Locate every blood parasite and identify its species.
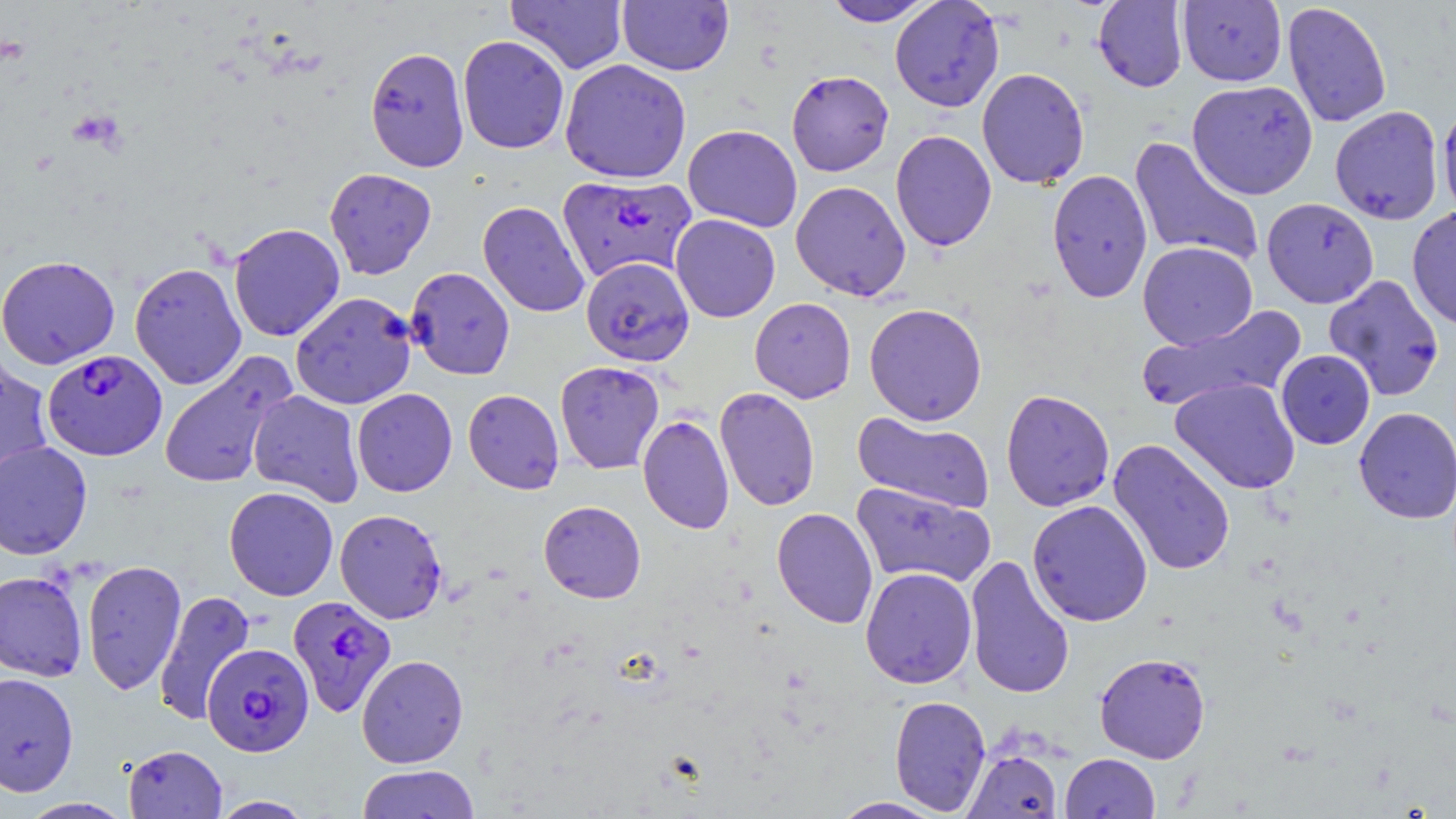
Approximate bounding boxes as (x1,y1)-(x2,y2) corner pairs in pixels.
Plasmodium falciparum-infected red blood cells: (557,174)-(696,283), (42,348)-(167,461), (288,595)-(397,717), (203,644)-(314,756).
No Plasmodium ovale, Plasmodium malariae, Plasmodium vivax, Babesia divergens, or Trypanosoma brucei observed.

Summary:
  - Uninfected red blood cell locations: (822,0)-(936,26), (890,0)-(1005,112), (1093,0)-(1188,92), (1177,0)-(1287,87), (505,1)-(628,74), (617,1)-(734,75), (1282,1)-(1392,128), (457,35)-(570,154), (365,46)-(470,172), (560,58)-(692,183), (976,67)-(1090,189), (786,70)-(894,176), (1187,80)-(1318,199), (1437,103)-(1456,221), (1330,106)-(1445,225), (683,124)-(802,232), (890,130)-(997,252), (1129,136)-(1265,269), (324,167)-(437,279), (1047,169)-(1153,302), (790,180)-(911,301), (1262,198)-(1379,308), (477,200)-(590,318), (1406,206)-(1456,330), (670,214)-(780,323), (228,223)-(346,342), (1137,241)-(1257,350), (0,255)-(120,369), (581,255)-(695,369), (129,262)-(247,390), (405,266)-(515,380), (1323,274)-(1445,401), (290,292)-(417,410), (749,297)-(856,403), (864,303)-(987,426), (1137,305)-(1306,413), (1275,349)-(1375,449), (158,352)-(295,490), (0,354)-(54,488), (555,361)-(665,474), (1170,377)-(1301,494), (714,387)-(820,511), (352,388)-(457,496), (1000,388)-(1115,512), (463,389)-(564,494), (248,390)-(365,507), (1354,407)-(1456,523), (852,412)-(995,515), (638,415)-(734,534), (1108,438)-(1236,577), (0,440)-(93,560), (852,482)-(996,589), (224,486)-(339,601), (1027,499)-(1153,627), (538,500)-(646,603), (771,507)-(878,629), (334,509)-(448,624), (964,554)-(1075,699), (81,559)-(186,695), (860,567)-(977,688), (0,570)-(88,682), (153,590)-(256,726), (1094,652)-(1211,764), (356,654)-(468,768), (0,671)-(79,797), (889,695)-(992,815), (123,744)-(227,818), (962,748)-(1062,818), (1060,753)-(1160,819), (357,764)-(480,818), (209,796)-(315,818), (18,797)-(135,818), (831,797)-(945,818)
  - Slide-level diagnosis: Plasmodium falciparum
  - Magnification: 1000x
  - Field of view: single
  - Preparation: thin blood film
  - Modality: light microscopy
  - Image size: 1456×819 pixels
  - Stain: May-Grünwald-Giemsa